Outline each P. falciparum parasite and classify it by life-cycle stage.
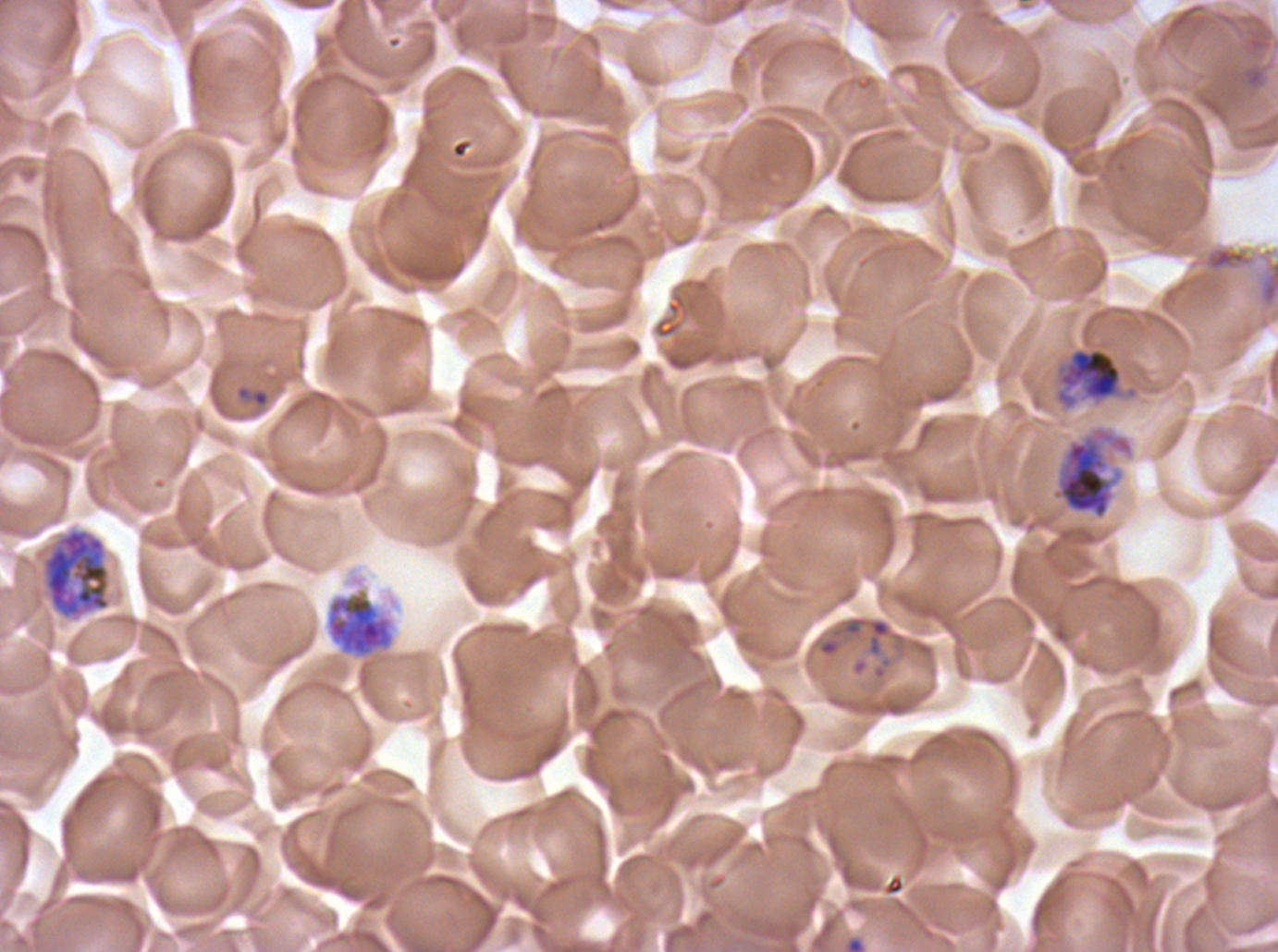

Approximate bounding rectangles given as corner coordinates in pixels from the top-left.
Rings: (x1=235, y1=384, x2=270, y2=409), (x1=841, y1=616, x2=891, y2=657).
Late trophozoites: (x1=1053, y1=346, x2=1124, y2=411).
Early schizonts: (x1=1050, y1=423, x2=1136, y2=521), (x1=43, y1=529, x2=111, y2=618), (x1=325, y1=587, x2=396, y2=660).
No late-ring/early-trophozoite forms, mid trophozoites, late schizonts, segmenters, or gametocytes observed.

Summary:
  - Debris locations: (x1=1205, y1=246, x2=1253, y2=273)
  - Stain: Giemsa
  - Life-cycle stages observed: ring, late trophozoite, early schizont
  - Preparation: thin blood smear
  - Field of view: sub-image separated from a larger composite
  - Specimen: P. falciparum from a patient in The Gambia, cultured ex vivo for 24 to 48 hours
  - Image size: 1278×952 pixels